Assess for Plasmodium parasites.
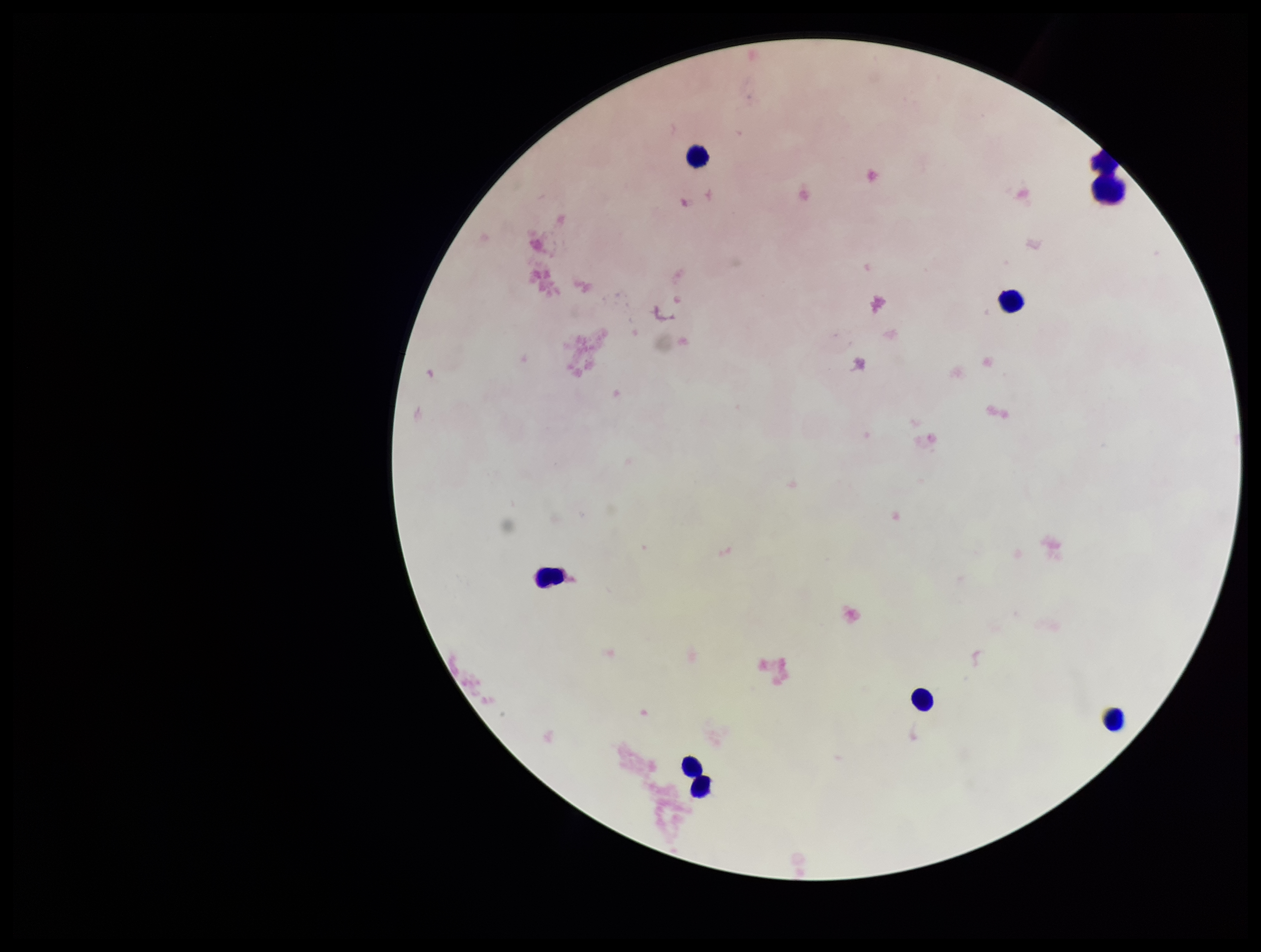

None detected.

leukocyte count = 8
image size = 1261×952 pixels
parasite count = 0
stain = Giemsa
field of view = one from this slide
capture = smartphone photograph through the microscope eyepiece
patient malaria status = negative
preparation = thick